Identify the parasite.
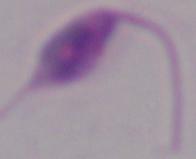
Leishmania.

Micrograph. 1000x magnification.